State which parasite is depicted.
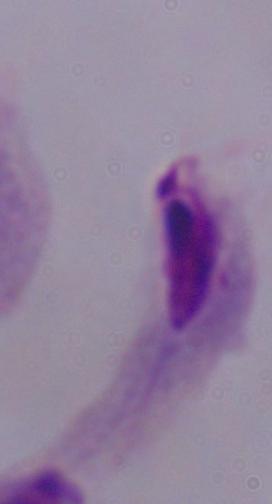
A trichomonad.

Micrograph. Captured at 1000x magnification.